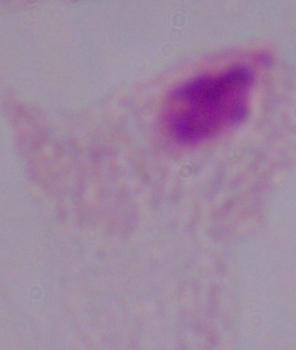

Micrograph. A trichomonad is shown. Captured at 1000x magnification.